Assess for Plasmodium parasites.
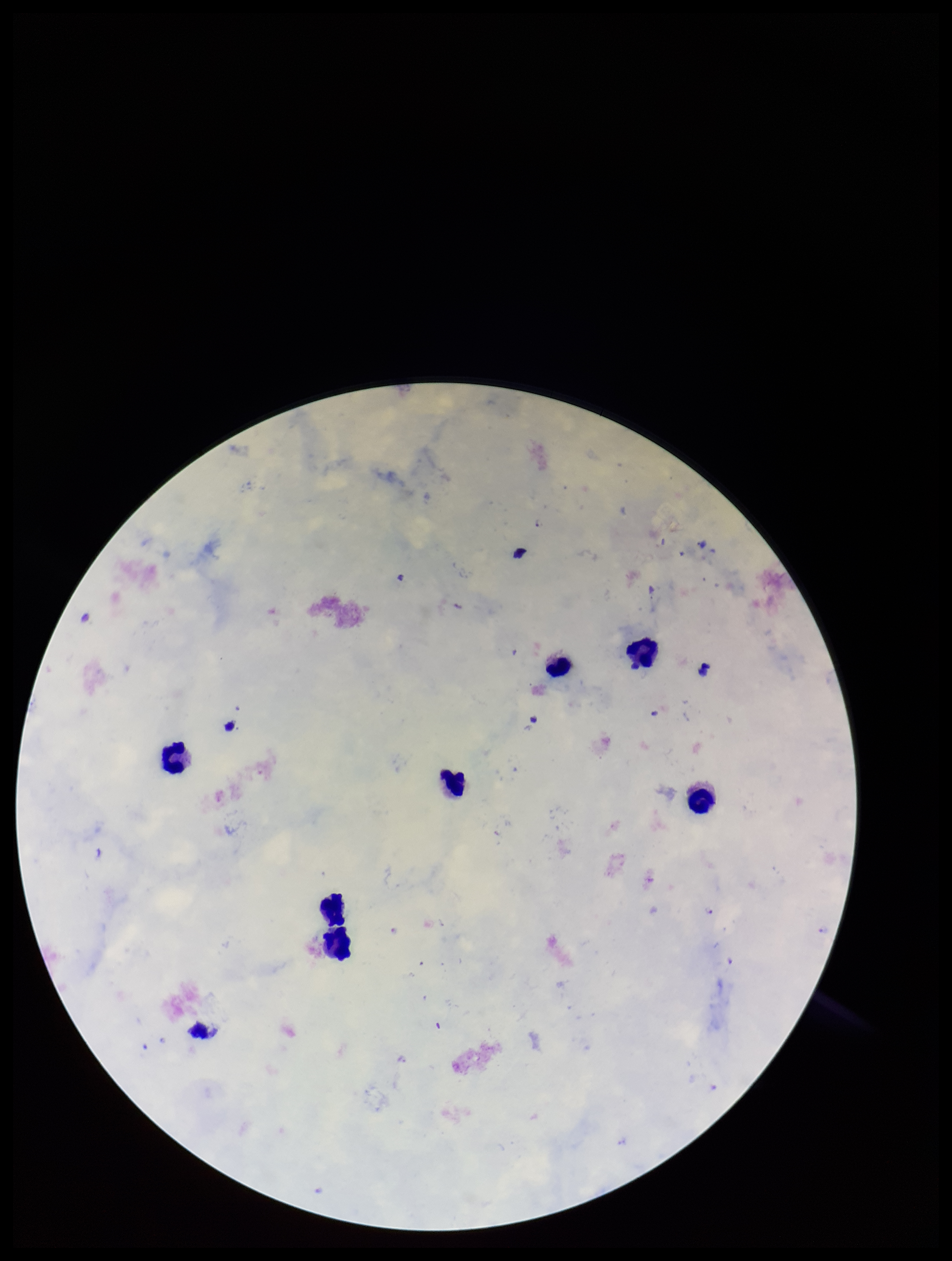
None identified.

Summary:
  - Stain: Giemsa
  - Preparation: thick smear
  - Field of view: one from this slide
  - Patient malaria status: infected
  - Parasite count: 0
  - Leukocyte count: 8
  - Species reported for this patient: Plasmodium falciparum
  - Capture: smartphone photograph through the microscope eyepiece
  - Image size: 952×1261 pixels